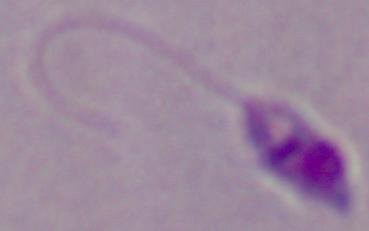 Photomicrograph. A Leishmania parasite is seen. 1000x magnification.